Locate every malaria parasite.
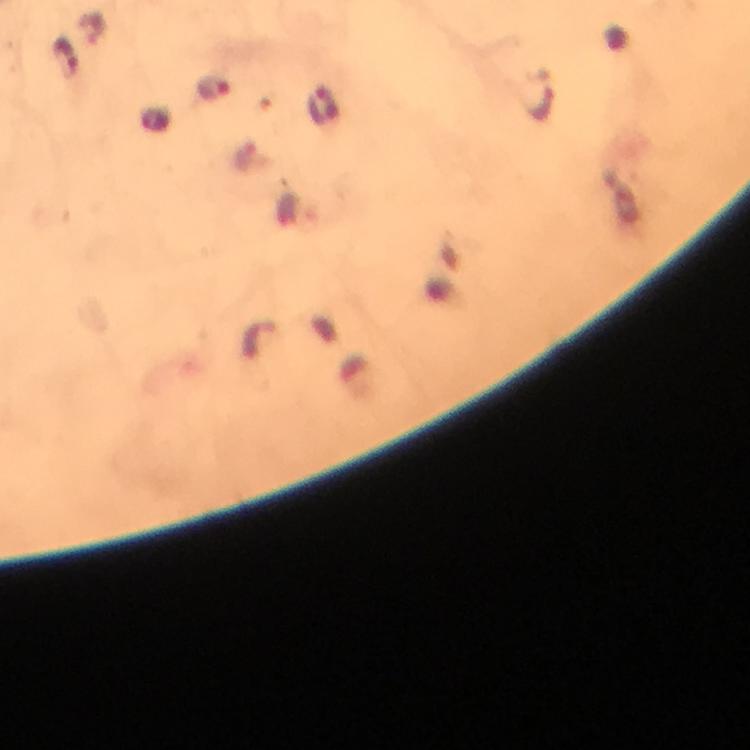

Approximate object centers, in pixels from the top-left corner.
Malaria parasites: (x=67, y=58), (x=216, y=89), (x=540, y=95).

Immersion oil was used. Giemsa stain. Image is 750×750 pixels. Cropped region of a single field of view. Photographed through the microscope with a smartphone camera. From a diagnostic examination for malaria. At 100x magnification. Thick smear.